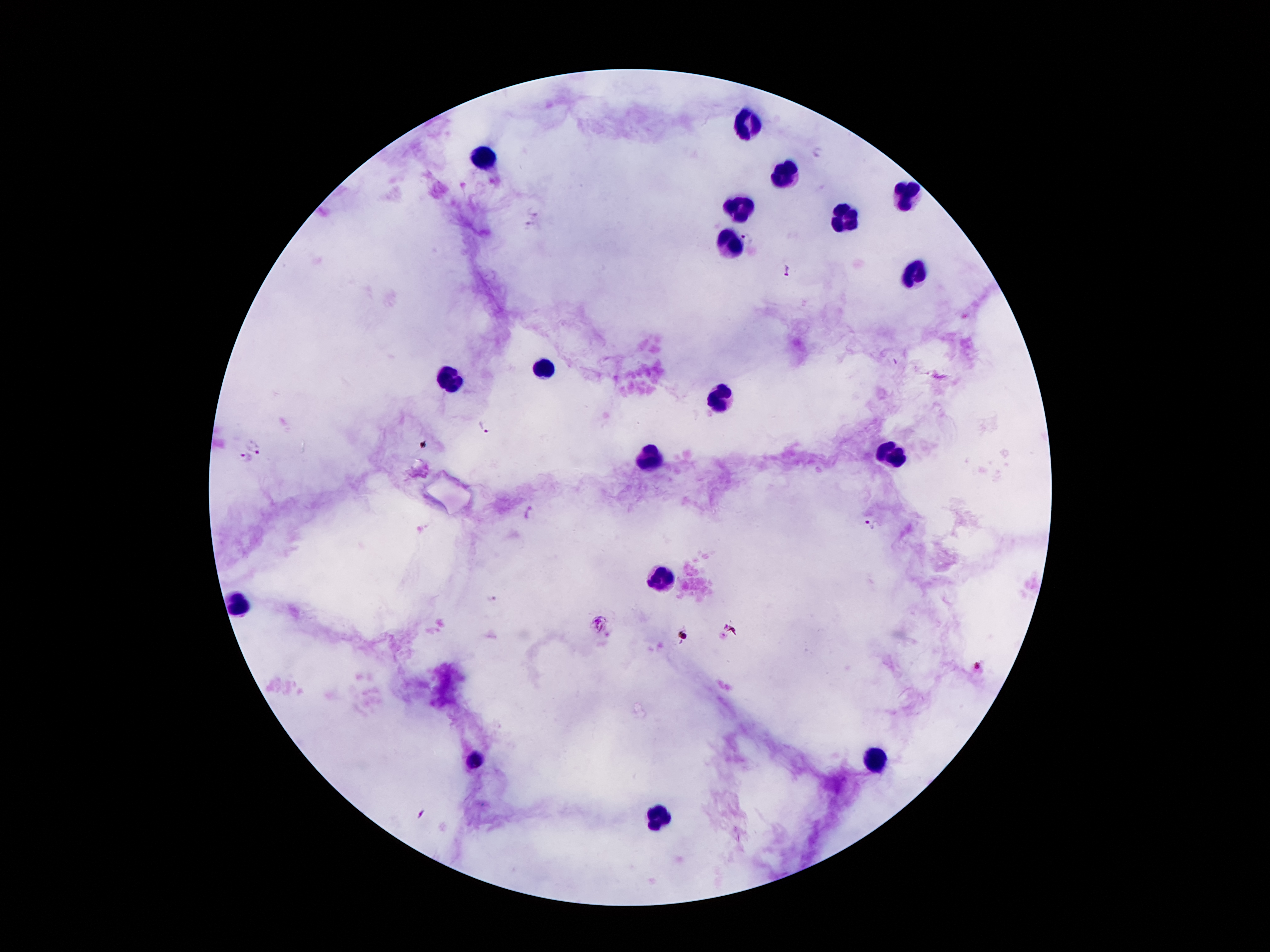 Approximate centers as (x, y) in pixels. Malaria parasite locations: (818, 152), (536, 209), (528, 226), (745, 238), (786, 267), (485, 427), (256, 447), (243, 458), (530, 513), (870, 525), (492, 600), (979, 669), (422, 813). Leukocyte locations: (749, 122), (483, 158), (787, 175), (908, 195), (738, 203), (848, 219), (728, 242), (912, 274), (547, 369), (451, 375), (715, 390), (888, 454), (653, 459), (662, 578), (239, 606), (877, 760), (477, 761), (660, 816). Thick blood smear. Image is 1270×952 pixels. 100x magnification. One field from this slide. Smartphone photograph taken through the microscope eyepiece. Patient malaria status: positive for Plasmodium falciparum. Giemsa stain.